Locate leukocytes (white blood cells).
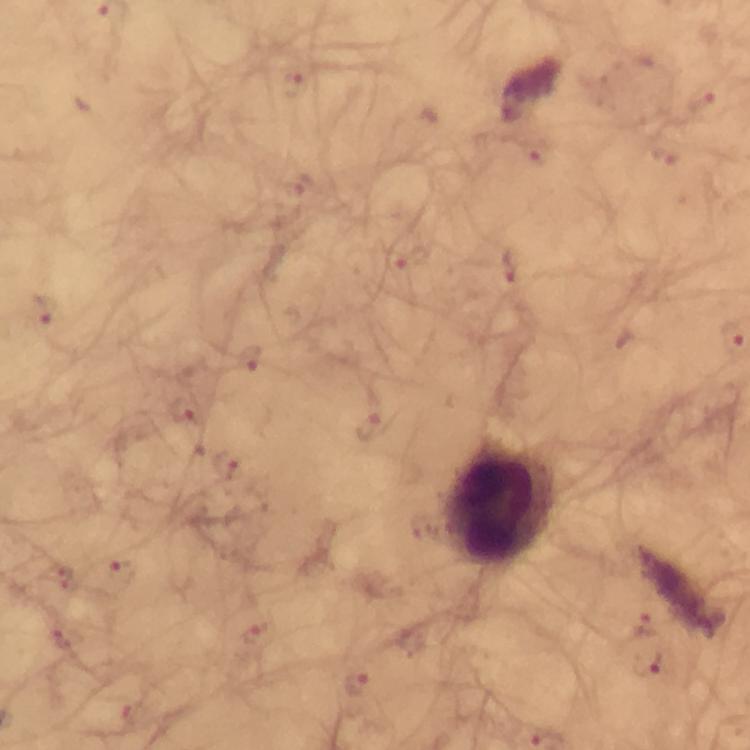
Approximate centers as [x, y] in pixels.
Leukocytes: [500, 506].

immersion oil = used
cropped from = one field of view
preparation = thick blood film
malaria parasite locations = approximate centers as [x, y] in pixels: [291, 81], [702, 99], [663, 153], [536, 155], [296, 185], [414, 257], [510, 266], [43, 312], [246, 359], [182, 412], [369, 428], [227, 466], [60, 574], [118, 576], [643, 628], [258, 631], [60, 635], [358, 684], [129, 718]
capture = smartphone mounted on the microscope
stain = Giemsa
magnification = 100x
image size = 750×750 pixels
context = from a malaria diagnostic workup